Name the parasite shown.
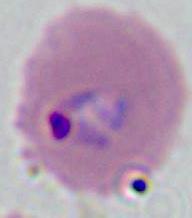
This is Plasmodium.

Summary:
  - Modality: micrograph
  - Magnification: 400x or 1000x